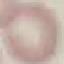
Result: no malaria parasites seen. Thin blood film. Giemsa stain. Acquired by smartphone through the microscope eyepiece. Cell patch, automatically extracted from a larger field of view and resized to 64 × 64 pixels.